Name the parasite shown.
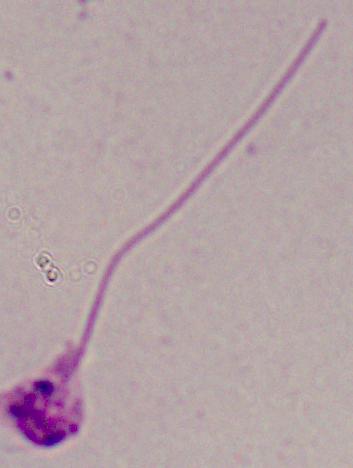

Leishmania.

Summary:
  - Magnification: 1000x
  - Modality: photomicrograph